Point out each malaria parasite and classify it by life-cycle stage.
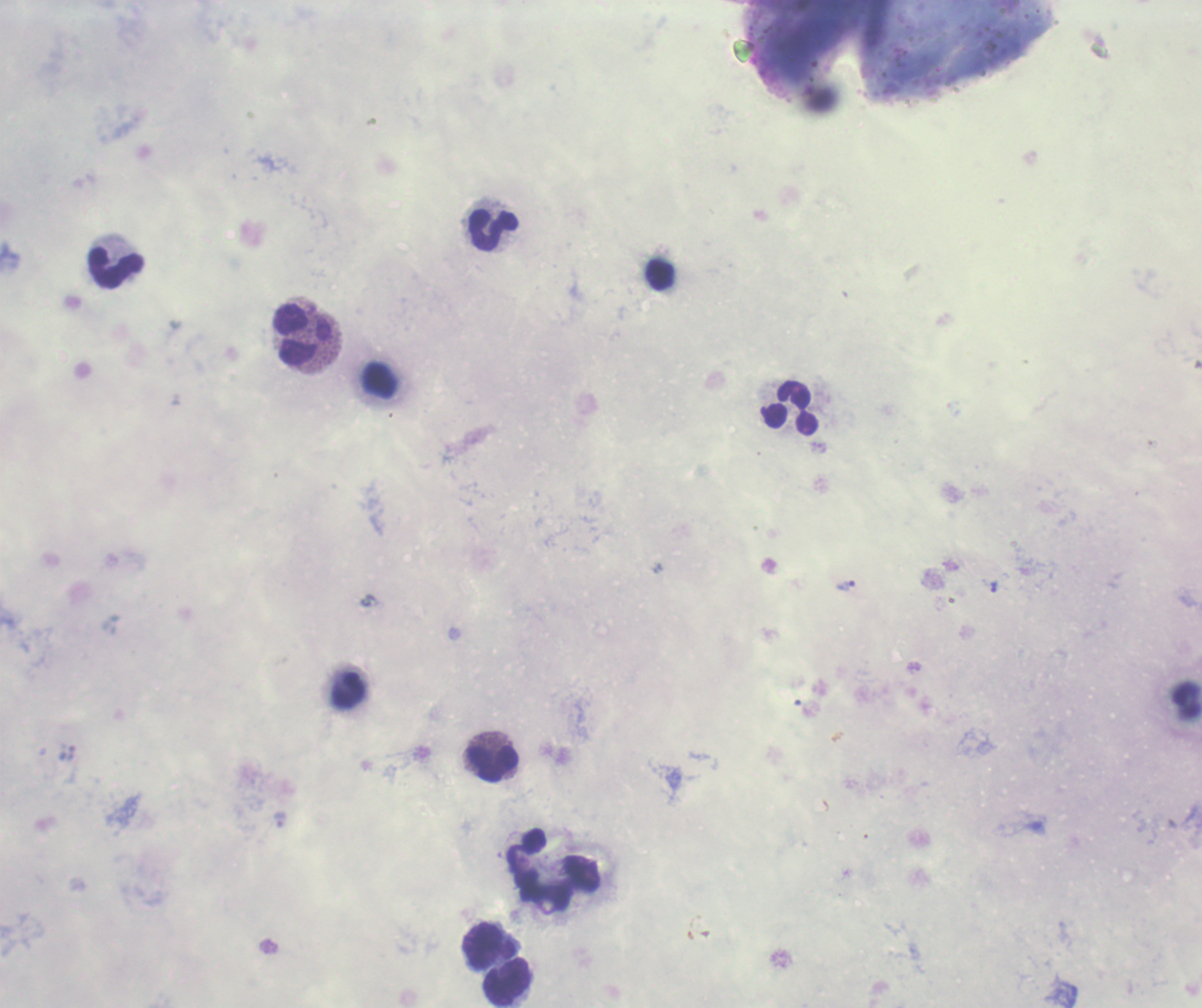
Approximate object centers, in pixels from the top-left corner.
Trophozoites: (x=846, y=586), (x=994, y=586), (x=280, y=820).
No schizont or gametocyte forms observed.

{
  "field_of_view": "single",
  "context": "previously used in a real diagnosis",
  "stain": "Romanowsky",
  "image_size": "1202×1008 pixels",
  "magnification": "100x",
  "leukocyte_locations": "approximate object centers, in pixels from the top-left corner: (x=494, y=231), (x=116, y=268), (x=660, y=275), (x=304, y=335), (x=792, y=409), (x=349, y=692), (x=494, y=764), (x=490, y=944), (x=509, y=983)",
  "coloration_quality": "bad",
  "background_quality": "poor",
  "preparation": "thick blood smear"
}